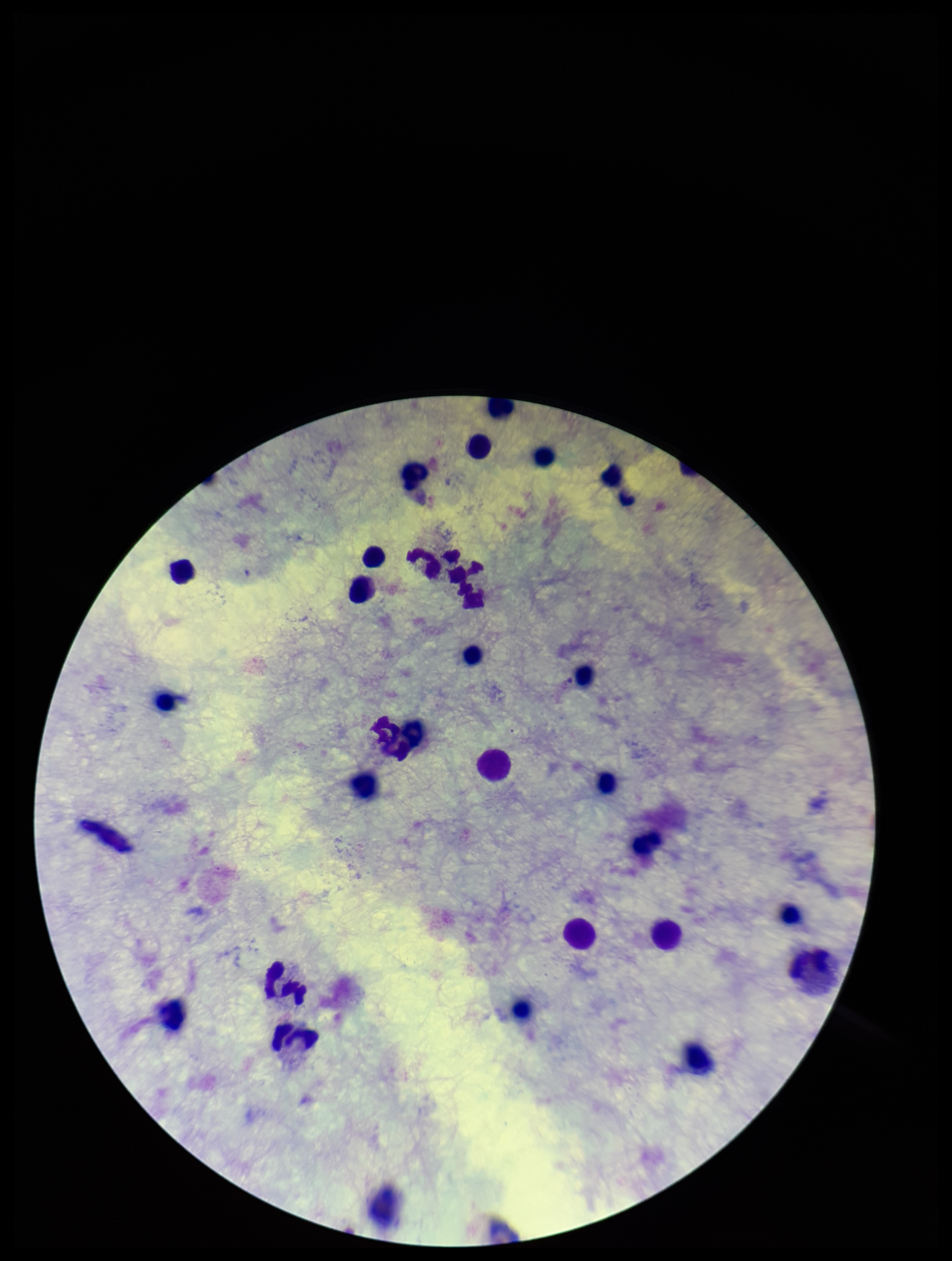

Image is 952×1261 pixels. Single field of view. Parasite count: 0. Plasmodium parasites: none identified. Photographed through the microscope eyepiece with a smartphone camera. Patient malaria status: negative. Preparation: thick. Stained with Giemsa. Leukocyte count: 28.